State the blood parasite species.
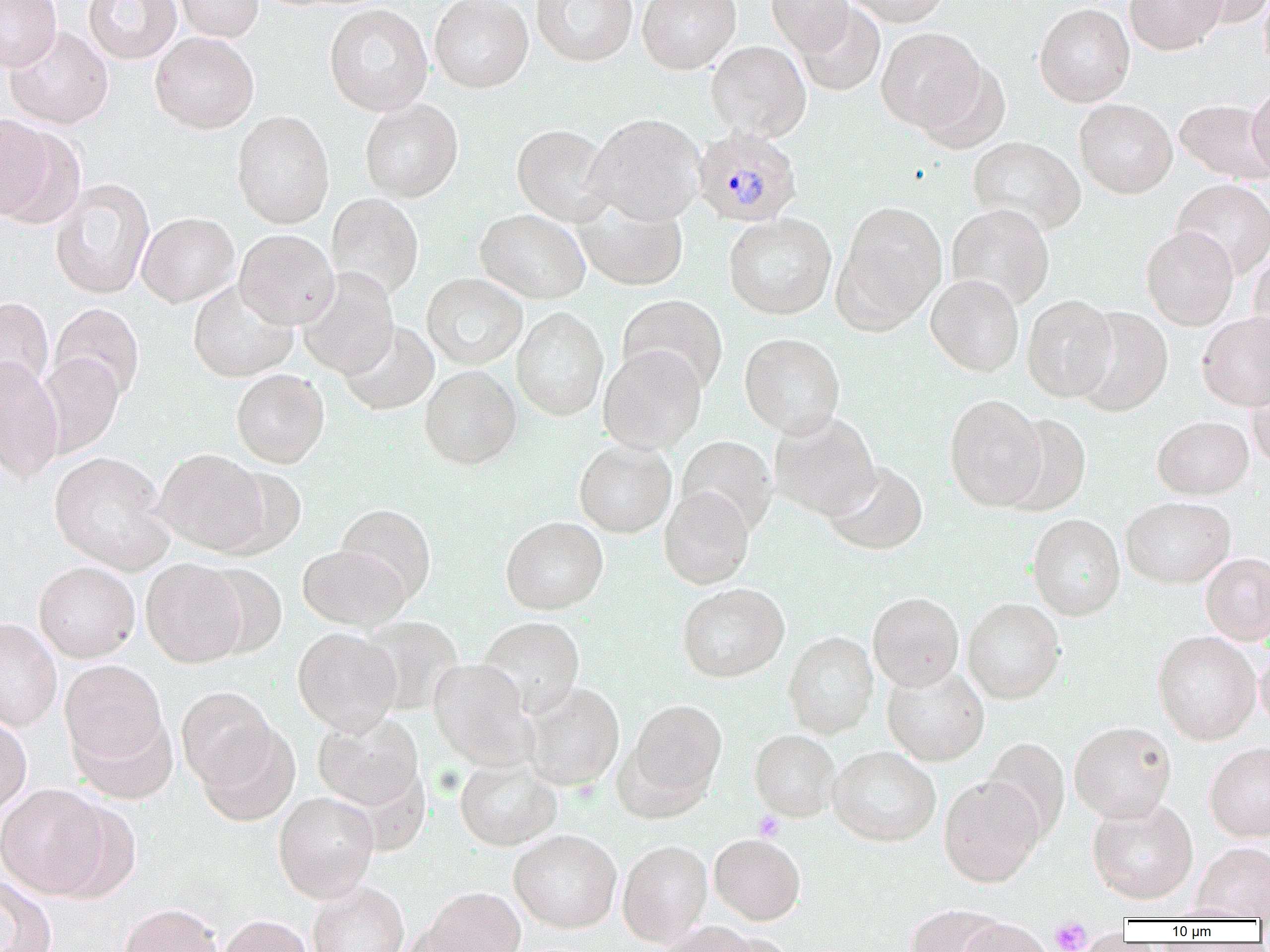
Plasmodium malariae.

Summary:
  - Coordinate format: approximate bounding boxes as (x1,y1)-(x2,y2) corner pairs in pixels
  - Platelet locations: (754,811)-(785,842), (1050,918)-(1092,952)
  - Uninfected red blood cell locations: (0,0)-(62,71), (84,0)-(182,64), (174,0)-(263,42), (429,0)-(533,93), (531,0)-(638,66), (637,0)-(741,74), (766,0)-(854,55), (845,0)-(949,26), (1124,0)-(1228,55), (1189,0)-(1270,27), (1259,0)-(1270,75), (795,2)-(885,96), (1034,3)-(1135,107), (324,4)-(433,116), (4,25)-(113,129), (876,27)-(984,131), (150,31)-(259,133), (706,40)-(811,142), (915,61)-(1010,154), (1247,83)-(1270,176), (1074,98)-(1177,198), (359,99)-(463,203), (1175,99)-(1269,184), (231,110)-(335,229), (586,113)-(706,225), (0,121)-(80,227), (511,123)-(616,227), (968,136)-(1086,235), (50,178)-(155,299), (1171,178)-(1270,280), (326,193)-(424,299), (571,199)-(688,292), (833,200)-(948,332), (946,203)-(1055,310), (475,208)-(590,304), (137,212)-(239,307), (723,212)-(837,320), (1141,227)-(1238,330), (235,229)-(339,329), (1248,249)-(1270,361), (297,268)-(399,379), (421,273)-(527,370), (925,274)-(1025,377), (188,279)-(298,382), (1021,294)-(1118,402), (617,295)-(728,395), (0,297)-(54,395), (50,303)-(144,402), (1072,306)-(1172,417), (512,307)-(609,420), (1197,312)-(1270,412), (339,321)-(440,415), (739,333)-(846,438), (598,345)-(707,454), (37,354)-(124,457), (0,355)-(64,483), (419,365)-(521,469), (231,369)-(330,468), (1246,369)-(1270,470), (944,393)-(1047,511), (768,411)-(880,521), (1001,413)-(1091,516), (1152,415)-(1254,500), (676,435)-(776,535), (574,440)-(677,538), (153,448)-(269,556), (49,451)-(173,574), (824,462)-(928,556), (216,464)-(307,559), (659,487)-(755,589), (1120,496)-(1235,588), (335,503)-(436,604), (1027,513)-(1125,620), (500,516)-(609,615), (297,544)-(409,631), (1200,552)-(1270,645), (141,558)-(247,668), (34,561)-(140,662), (200,564)-(287,658), (677,583)-(789,683), (867,592)-(964,692), (962,598)-(1065,704), (359,615)-(464,715), (477,616)-(585,718), (0,617)-(62,731), (293,627)-(402,735), (1152,631)-(1261,745), (783,632)-(879,738), (1255,642)-(1270,732), (428,658)-(536,770), (60,661)-(170,770), (881,664)-(989,766), (520,681)-(625,791), (175,685)-(278,791), (626,699)-(727,804), (71,711)-(178,804), (313,711)-(424,812), (0,715)-(31,819), (195,721)-(300,826), (1069,721)-(1177,823), (749,729)-(841,822), (981,738)-(1070,842), (1204,742)-(1270,842), (828,746)-(941,846), (454,758)-(562,851), (939,776)-(1045,888), (0,784)-(112,899), (273,791)-(379,902), (1087,798)-(1199,904), (508,830)-(622,932), (708,833)-(806,925), (617,839)-(713,946), (1193,842)-(1270,920), (0,877)-(57,952), (307,881)-(409,952), (421,886)-(526,952), (118,903)-(224,952), (904,905)-(1008,952), (218,915)-(315,952), (956,919)-(1055,952), (654,921)-(761,952)
  - Plasmodium malariae-infected red blood cell locations: (692,125)-(803,227)
  - Magnification: 1000x
  - Field of view: single
  - Modality: optical microscopy
  - Preparation: thin blood film
  - Image size: 1270×952 pixels